Give the extent of all Plasmodium parasites.
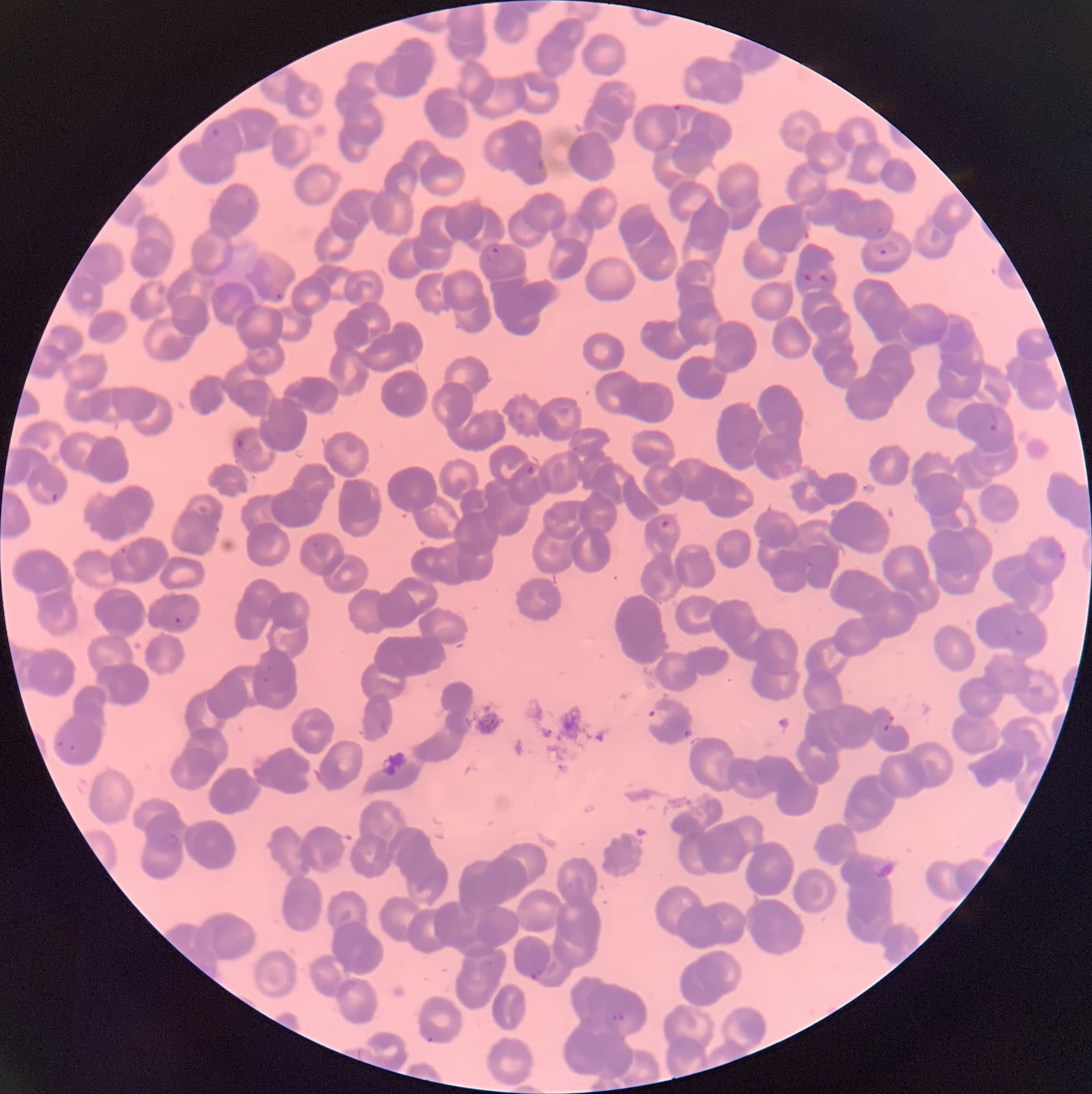

Approximate bounding boxes as (x1, y1, x2, y2) in pixels.
Plasmodium parasites: (670, 104, 682, 112), (211, 128, 220, 137), (874, 242, 900, 255), (483, 248, 502, 264), (798, 270, 835, 284), (273, 293, 285, 299), (990, 415, 998, 431), (233, 436, 249, 451), (523, 464, 539, 479), (48, 491, 61, 505), (658, 519, 677, 534), (309, 539, 332, 558), (120, 547, 128, 553), (173, 616, 196, 626), (1013, 623, 1026, 639), (263, 665, 272, 682), (643, 705, 669, 729), (883, 713, 894, 733), (55, 741, 76, 754), (159, 832, 180, 848), (529, 965, 546, 980), (610, 1013, 625, 1021), (423, 1034, 436, 1044).

image size = 1092×1094 pixels
red blood cell morphology = rouleaux formation
preparation = thin blood film
modality = optical microscopy